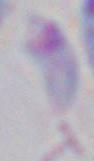

Summary:
  - Identification: Toxoplasma gondii
  - Magnification: 1000x
  - Modality: micrograph